Give the position of every leukocyte visible.
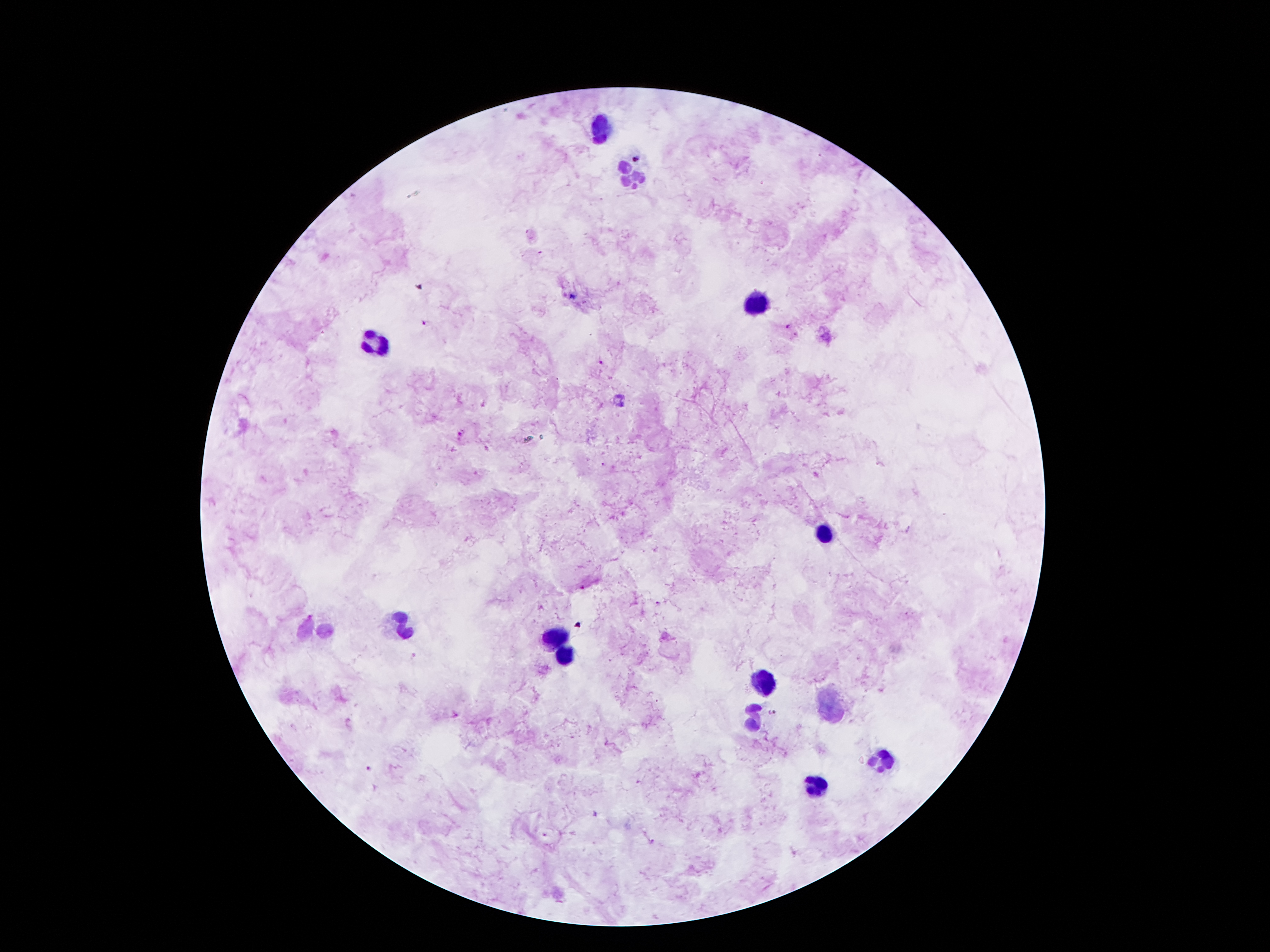

Approximate centers as [x, y] in pixels.
Leukocytes: [597, 127], [634, 173], [752, 307], [378, 340], [825, 535], [404, 628], [313, 629], [556, 637], [564, 656], [758, 682], [832, 705], [752, 716], [884, 761], [813, 786].

Plasmodium parasite locations: [422, 324], [788, 329], [600, 363], [459, 434], [774, 714], [369, 769]. Patient malaria status: infected with Plasmodium falciparum. One field from this slide. Giemsa stain. Thick blood smear. Photographed through the microscope eyepiece with a smartphone camera. 100x magnification. Image is 1270×952 pixels.